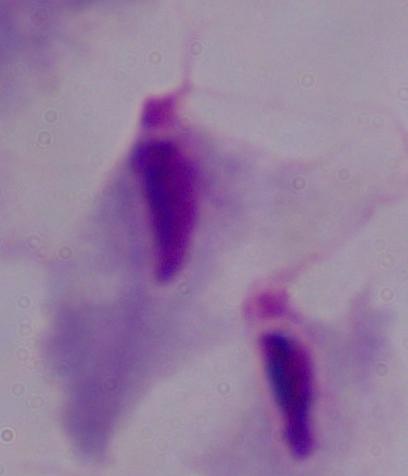

{
  "modality": "photomicrograph",
  "identification": "trichomonad",
  "magnification": "1000x"
}